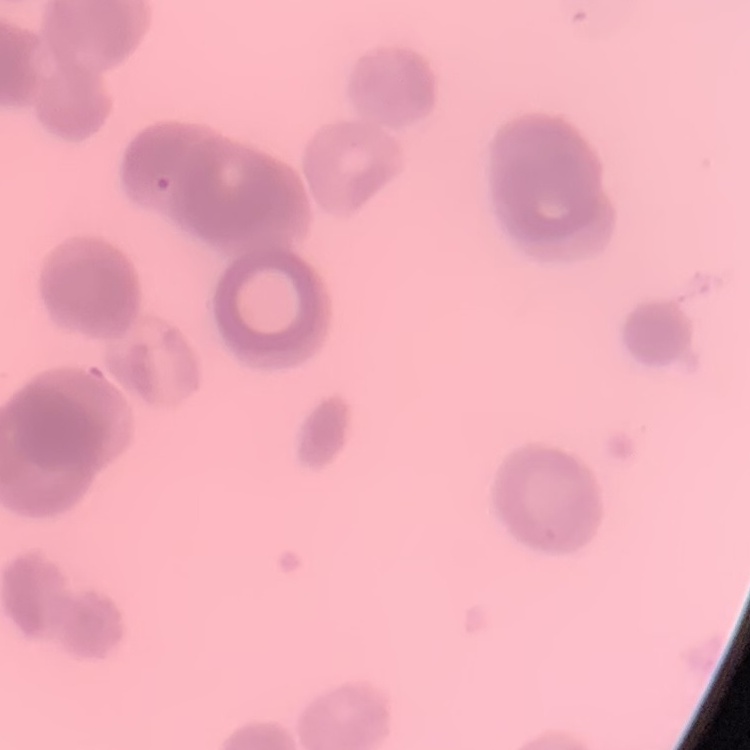

The erythrocytes exhibit rouleaux formation. Thin peripheral smear. Field's or Giemsa stain. Square crop of a larger photomicrograph.